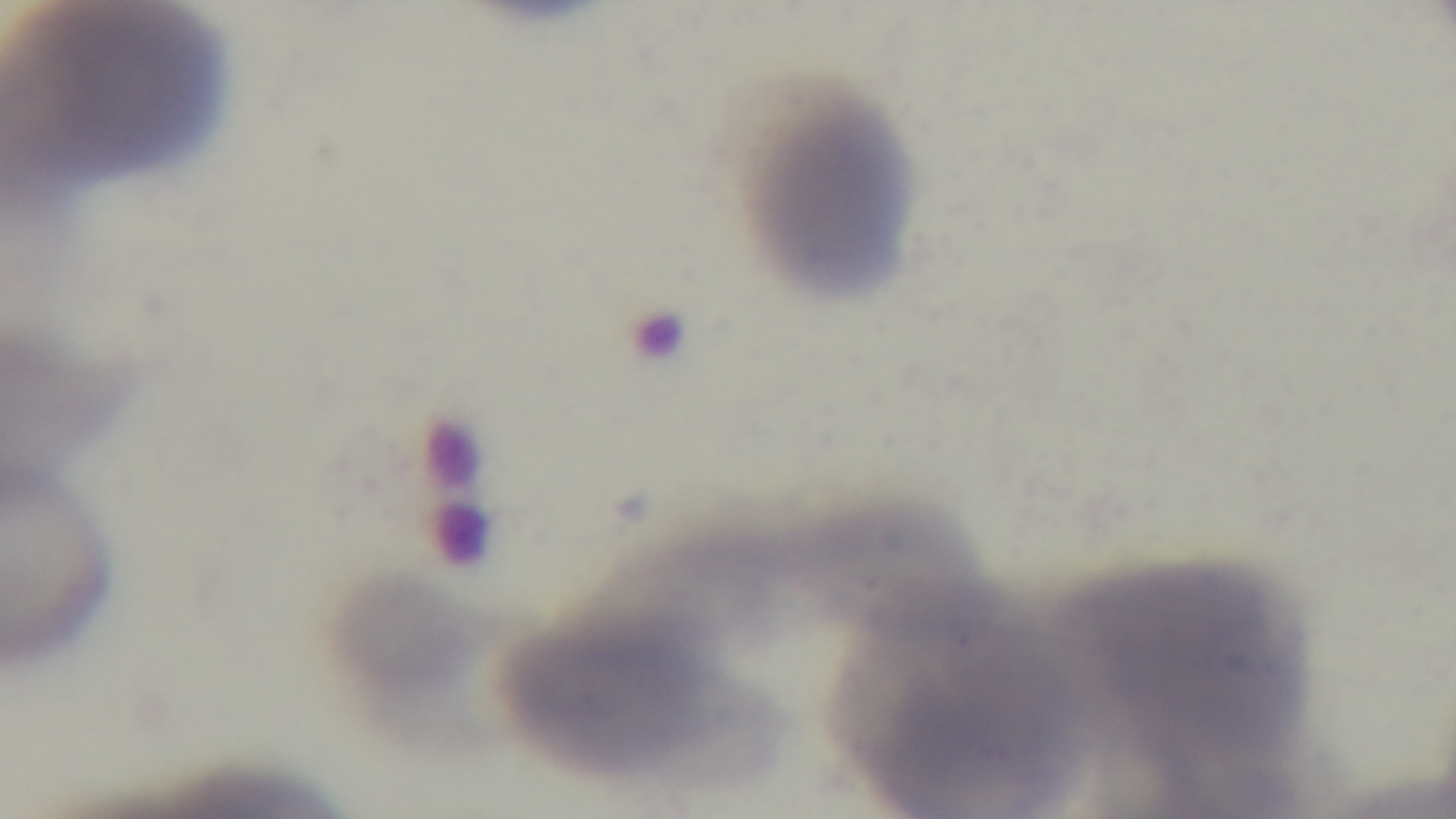
objective = 100x oil immersion
field of view = one from the slide
capture = mounted 4K digital camera
modality = light microscopy
preparation = thin
malaria status = uninfected
stain = Giemsa